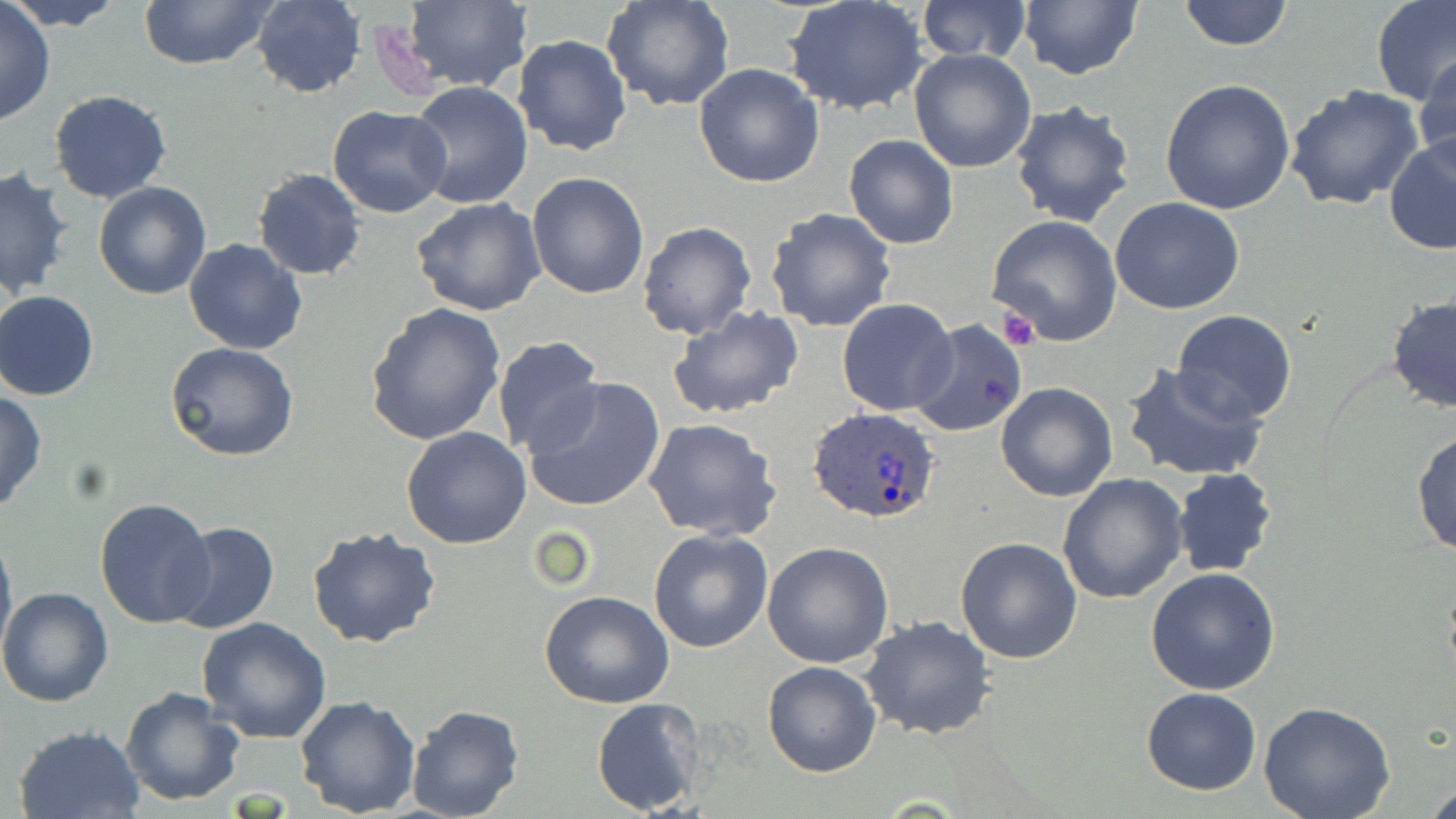
Summary:
  - Coordinate format: approximate bounding boxes as [x1, y1, x2, y2] in pixels
  - Plasmodium ovale-infected red blood cell locations: [808, 407, 942, 525]
  - Platelet locations: [996, 309, 1040, 350]
  - Uninfected red blood cell locations: [6, 0, 128, 30], [137, 0, 279, 71], [917, 0, 1032, 65], [1178, 0, 1293, 50], [1370, 0, 1455, 108], [0, 1, 56, 125], [248, 1, 367, 96], [398, 1, 533, 94], [784, 1, 931, 118], [1017, 1, 1144, 79], [603, 2, 733, 111], [512, 33, 633, 156], [909, 48, 1037, 173], [1414, 53, 1456, 173], [693, 63, 825, 188], [1159, 79, 1297, 215], [404, 82, 532, 210], [1284, 85, 1426, 211], [49, 91, 173, 205], [1009, 100, 1138, 229], [328, 105, 452, 216], [1383, 133, 1456, 256], [843, 134, 959, 249], [1, 168, 74, 300], [251, 168, 367, 280], [526, 171, 650, 298], [94, 182, 211, 299], [412, 198, 547, 317], [1109, 198, 1244, 315], [763, 207, 897, 333], [986, 216, 1123, 345], [636, 220, 757, 340], [183, 237, 307, 354], [1, 290, 99, 400], [1385, 296, 1456, 416], [837, 299, 958, 417], [366, 304, 505, 444], [666, 306, 806, 422], [1171, 310, 1297, 425], [908, 317, 1030, 437], [493, 335, 607, 459], [167, 342, 298, 462], [1121, 363, 1268, 483], [523, 378, 665, 513], [994, 382, 1118, 502], [0, 390, 47, 512], [643, 418, 783, 541], [401, 426, 532, 549], [1411, 429, 1456, 555], [1171, 467, 1276, 577], [1057, 475, 1188, 605], [94, 497, 218, 630], [171, 522, 280, 635], [0, 523, 16, 664], [307, 526, 441, 648], [647, 528, 773, 653], [954, 536, 1084, 663], [762, 541, 893, 668], [1146, 567, 1281, 696], [0, 586, 113, 708], [538, 591, 674, 710], [860, 614, 996, 741], [197, 617, 331, 742], [762, 660, 882, 778], [120, 687, 245, 806], [1140, 687, 1263, 795], [294, 695, 421, 817], [591, 697, 707, 816], [1259, 703, 1395, 819], [406, 704, 524, 819], [14, 724, 147, 818]
  - Slide-level diagnosis: Plasmodium ovale
  - Field of view: one of a larger specimen
  - Stain: May-Grünwald-Giemsa
  - Image size: 1456×819 pixels
  - Magnification: 1000x
  - Modality: light microscopy
  - Preparation: thin blood film